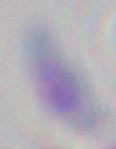

identification = Toxoplasma gondii
modality = photomicrograph
magnification = 1000x